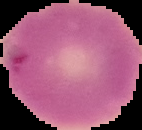
Image is 142×130 pixels. From a thin blood film. Segmented cell region on a black background. Malaria status: uninfected.